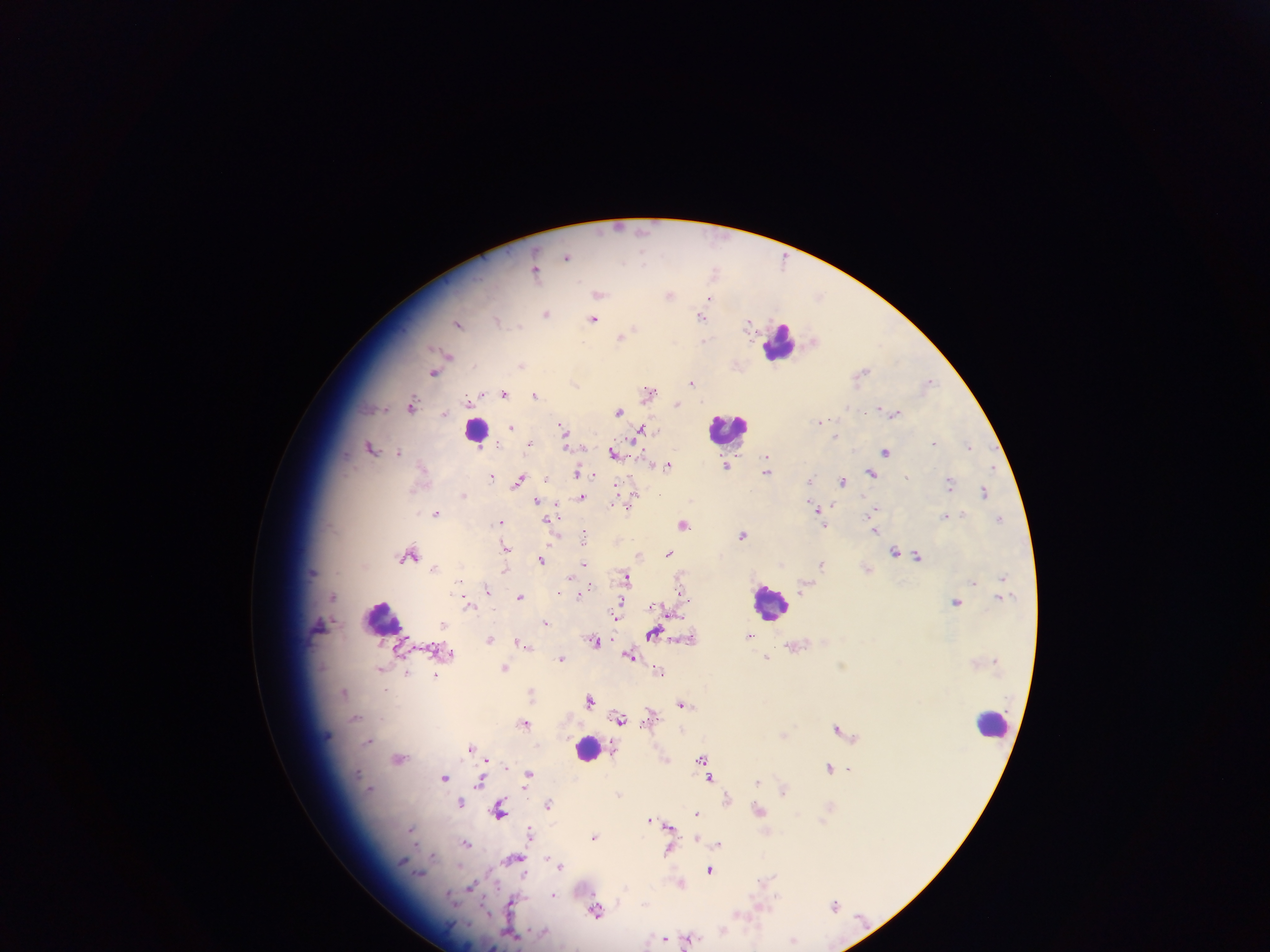
field of view = single
preparation = thick blood smear
leukocyte locations = approximate centers as {x, y} in pixels: {780, 343}, {729, 427}, {476, 430}, {771, 601}, {384, 618}, {993, 724}, {588, 749}
country = Ghana
capture = mobile-phone photograph through a microscope
malaria parasite locations = approximate centers as {x, y} in pixels: {644, 231}, {566, 256}, {643, 257}, {536, 271}, {714, 271}, {599, 294}, {669, 294}, {821, 296}, {710, 298}, {546, 313}, {702, 316}, {594, 319}, {499, 321}, {749, 323}, {458, 324}, {634, 327}, {620, 336}, {705, 340}, {814, 340}, {449, 355}, {522, 366}, {435, 372}, {862, 373}, {574, 382}, {692, 382}, {928, 383}, {648, 390}, {505, 393}, {477, 395}, {536, 395}, {468, 399}, {677, 403}, {412, 404}, {847, 407}, {883, 409}, {618, 411}, {895, 413}, {444, 414}, {823, 421}, {511, 427}, {563, 430}, {641, 431}, {835, 435}, {565, 437}, {530, 443}, {934, 443}, {969, 445}, {372, 446}, {399, 452}, {614, 452}, {886, 452}, {767, 455}, {421, 465}, {667, 465}, {727, 465}, {578, 471}, {768, 471}, {871, 473}, {492, 476}, {907, 477}, {547, 478}, {519, 480}, {810, 480}, {843, 481}, {951, 483}, {985, 492}, {463, 494}, {581, 496}, {632, 499}, {537, 501}, {612, 504}, {817, 509}, {872, 511}, {436, 513}, {946, 515}, {1000, 519}, {501, 521}, {550, 521}, {683, 524}, {875, 530}, {584, 535}, {742, 535}, {505, 548}, {669, 552}, {896, 552}, {409, 555}, {638, 555}, {918, 555}, {541, 560}, {584, 564}, {822, 564}, {435, 568}, {505, 569}, {571, 575}, {1002, 576}, {626, 577}, {680, 580}, {974, 582}, {487, 588}, {586, 588}, {804, 588}, {582, 592}, {680, 593}, {334, 596}, {520, 597}, {956, 601}, {467, 603}, {617, 614}, {546, 622}, {654, 633}, {750, 636}, {489, 639}, {595, 640}, {522, 644}, {527, 646}, {450, 654}, {630, 655}, {562, 658}, {767, 658}, {504, 667}, {381, 670}, {659, 671}, {408, 673}, {436, 675}, {344, 691}, {532, 692}, {590, 699}, {682, 704}, {355, 718}, {620, 718}, {524, 722}, {838, 728}, {785, 734}, {369, 740}, {471, 747}, {399, 758}, {486, 759}, {702, 759}, {830, 767}, {528, 775}, {445, 777}, {710, 778}, {481, 782}, {757, 782}, {784, 790}, {619, 795}, {727, 798}, {461, 801}, {548, 804}, {500, 810}, {758, 810}, {697, 813}, {651, 819}, {669, 825}, {411, 829}, {530, 832}, {594, 837}, {697, 839}, {466, 843}, {719, 843}, {668, 851}, {433, 855}, {512, 858}, {548, 858}, {402, 861}, {560, 865}, {710, 870}, {525, 875}, {767, 879}, {681, 883}, {471, 887}, {554, 894}, {513, 902}, {834, 906}, {596, 911}, {739, 914}, {722, 931}, {512, 935}, {663, 938}, {691, 938}, {793, 939}
image size = 1270×952 pixels